Name the parasite shown.
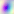
Toxoplasma gondii.

Captured at 400x magnification. Micrograph.